Name the blood parasite species.
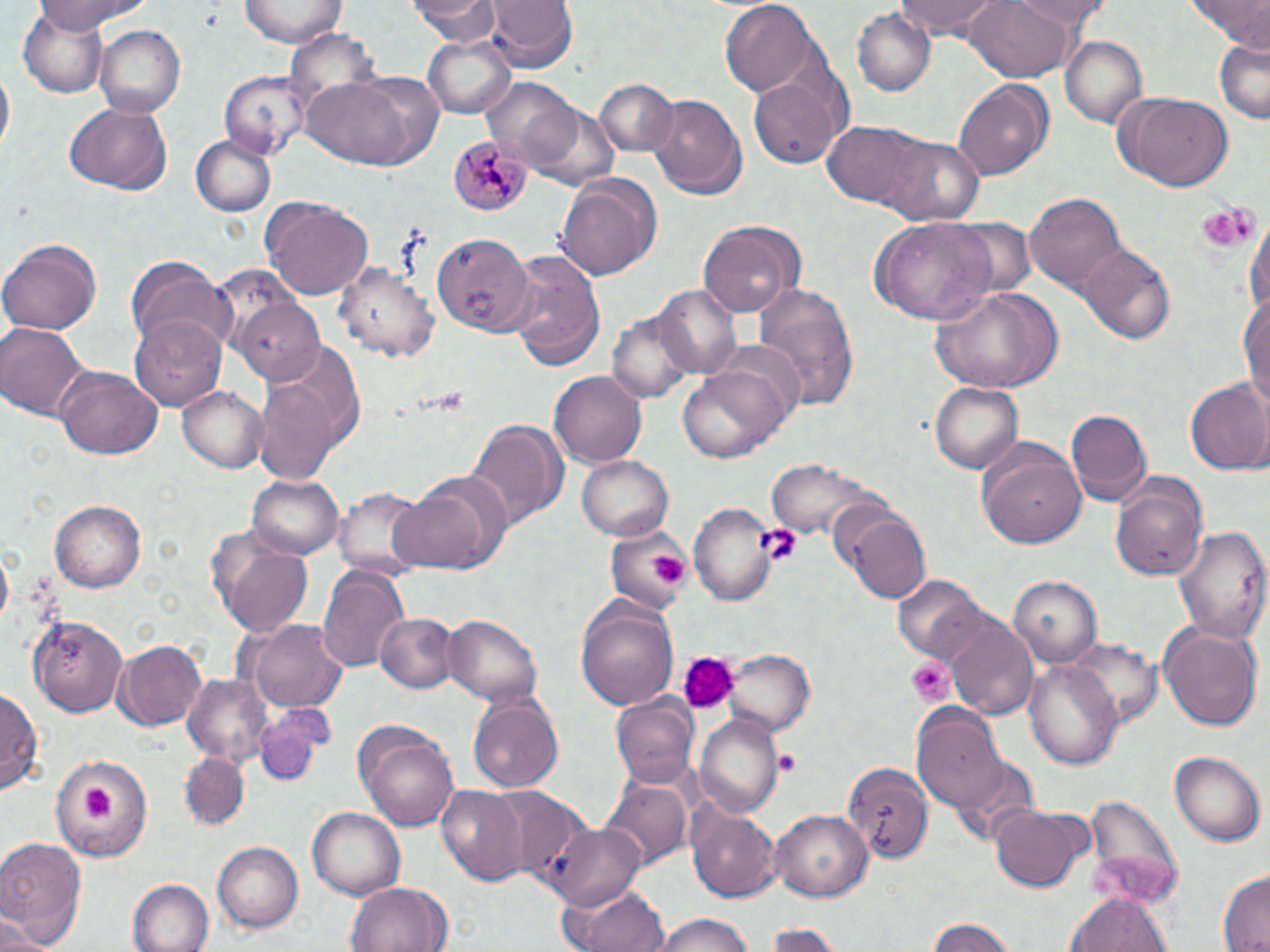

Plasmodium malariae.

{
  "uninfected_red_blood_cell_locations": "approximate bounding boxes as named x1/y1/x2/y2 corners in pixels: (x1=28, y1=0, x2=155, y2=34), (x1=240, y1=0, x2=346, y2=48), (x1=408, y1=0, x2=503, y2=44), (x1=897, y1=0, x2=1007, y2=41), (x1=963, y1=0, x2=1079, y2=83), (x1=1007, y1=0, x2=1112, y2=29), (x1=1190, y1=0, x2=1270, y2=50), (x1=485, y1=1, x2=577, y2=72), (x1=721, y1=1, x2=819, y2=94), (x1=19, y1=7, x2=111, y2=97), (x1=852, y1=8, x2=935, y2=96), (x1=96, y1=25, x2=184, y2=117), (x1=421, y1=34, x2=517, y2=119), (x1=1059, y1=35, x2=1147, y2=128), (x1=1213, y1=37, x2=1269, y2=125), (x1=1, y1=64, x2=15, y2=158), (x1=218, y1=71, x2=309, y2=161), (x1=296, y1=74, x2=438, y2=169), (x1=748, y1=75, x2=843, y2=170), (x1=482, y1=78, x2=583, y2=170), (x1=593, y1=78, x2=680, y2=157), (x1=954, y1=78, x2=1054, y2=180), (x1=1114, y1=91, x2=1233, y2=193), (x1=646, y1=93, x2=748, y2=202), (x1=64, y1=104, x2=172, y2=195), (x1=823, y1=121, x2=930, y2=210), (x1=189, y1=136, x2=276, y2=216), (x1=879, y1=138, x2=983, y2=222), (x1=556, y1=171, x2=663, y2=280), (x1=1026, y1=193, x2=1127, y2=294), (x1=261, y1=197, x2=374, y2=300), (x1=1245, y1=215, x2=1270, y2=323), (x1=951, y1=216, x2=1036, y2=297), (x1=868, y1=218, x2=1001, y2=325), (x1=699, y1=220, x2=803, y2=315), (x1=432, y1=230, x2=535, y2=333), (x1=1, y1=238, x2=103, y2=334), (x1=1078, y1=244, x2=1175, y2=345), (x1=504, y1=249, x2=605, y2=370), (x1=126, y1=257, x2=235, y2=352), (x1=337, y1=259, x2=440, y2=366), (x1=754, y1=281, x2=861, y2=412), (x1=931, y1=283, x2=1063, y2=393), (x1=654, y1=284, x2=742, y2=378), (x1=1239, y1=292, x2=1270, y2=419), (x1=232, y1=297, x2=323, y2=381), (x1=610, y1=309, x2=694, y2=403), (x1=131, y1=313, x2=228, y2=411), (x1=0, y1=320, x2=89, y2=424), (x1=254, y1=340, x2=363, y2=482), (x1=677, y1=358, x2=796, y2=465), (x1=56, y1=366, x2=163, y2=460), (x1=550, y1=371, x2=646, y2=468), (x1=928, y1=379, x2=1023, y2=473), (x1=1185, y1=380, x2=1270, y2=475), (x1=178, y1=387, x2=266, y2=472), (x1=1066, y1=409, x2=1151, y2=506), (x1=465, y1=418, x2=567, y2=527), (x1=972, y1=436, x2=1083, y2=545), (x1=578, y1=455, x2=674, y2=540), (x1=767, y1=457, x2=893, y2=548), (x1=390, y1=469, x2=514, y2=575), (x1=248, y1=475, x2=342, y2=559), (x1=1112, y1=482, x2=1208, y2=583), (x1=334, y1=486, x2=432, y2=577), (x1=52, y1=499, x2=146, y2=593), (x1=829, y1=500, x2=931, y2=603), (x1=686, y1=504, x2=779, y2=604), (x1=1174, y1=524, x2=1267, y2=645), (x1=604, y1=528, x2=692, y2=613), (x1=211, y1=530, x2=315, y2=639), (x1=318, y1=565, x2=410, y2=670), (x1=1007, y1=575, x2=1101, y2=667), (x1=894, y1=577, x2=988, y2=663), (x1=576, y1=597, x2=679, y2=710), (x1=29, y1=613, x2=127, y2=715), (x1=378, y1=613, x2=457, y2=693), (x1=441, y1=615, x2=543, y2=702), (x1=944, y1=617, x2=1036, y2=719), (x1=246, y1=619, x2=350, y2=715), (x1=1160, y1=622, x2=1262, y2=734), (x1=113, y1=641, x2=207, y2=729), (x1=724, y1=650, x2=814, y2=735), (x1=1026, y1=662, x2=1123, y2=767), (x1=182, y1=673, x2=276, y2=768), (x1=0, y1=685, x2=41, y2=798), (x1=467, y1=692, x2=564, y2=794), (x1=613, y1=695, x2=700, y2=791), (x1=254, y1=707, x2=332, y2=787), (x1=913, y1=709, x2=1007, y2=811), (x1=695, y1=714, x2=784, y2=818), (x1=352, y1=719, x2=460, y2=832), (x1=1170, y1=750, x2=1264, y2=846), (x1=178, y1=753, x2=250, y2=832), (x1=56, y1=755, x2=149, y2=860), (x1=844, y1=763, x2=933, y2=865), (x1=600, y1=781, x2=690, y2=871), (x1=437, y1=785, x2=530, y2=886), (x1=490, y1=789, x2=597, y2=888), (x1=1083, y1=793, x2=1185, y2=907), (x1=688, y1=804, x2=782, y2=905), (x1=991, y1=804, x2=1086, y2=892), (x1=308, y1=807, x2=404, y2=899), (x1=768, y1=810, x2=874, y2=902), (x1=544, y1=821, x2=644, y2=911), (x1=0, y1=837, x2=87, y2=949), (x1=212, y1=840, x2=305, y2=933), (x1=1215, y1=871, x2=1269, y2=952), (x1=129, y1=879, x2=213, y2=952), (x1=345, y1=880, x2=455, y2=952), (x1=560, y1=882, x2=671, y2=952), (x1=1068, y1=893, x2=1171, y2=952), (x1=0, y1=911, x2=46, y2=952), (x1=649, y1=914, x2=764, y2=952), (x1=926, y1=918, x2=1018, y2=951), (x1=762, y1=923, x2=846, y2=951)",
  "image_size": "1270×952 pixels",
  "field_of_view": "single",
  "platelet_locations": "approximate bounding boxes as named x1/y1/x2/y2 corners in pixels: (x1=1195, y1=206, x2=1256, y2=252), (x1=756, y1=524, x2=800, y2=565), (x1=643, y1=551, x2=692, y2=587), (x1=683, y1=655, x2=739, y2=710), (x1=905, y1=655, x2=956, y2=706), (x1=773, y1=751, x2=804, y2=778), (x1=79, y1=785, x2=119, y2=821)",
  "preparation": "thin blood smear",
  "stain": "May-Grünwald-Giemsa",
  "plasmodium_malariae_infected_red_blood_cell_locations": "approximate bounding boxes as named x1/y1/x2/y2 corners in pixels: (x1=448, y1=136, x2=529, y2=218)",
  "magnification": "1000x",
  "modality": "optical microscopy"
}